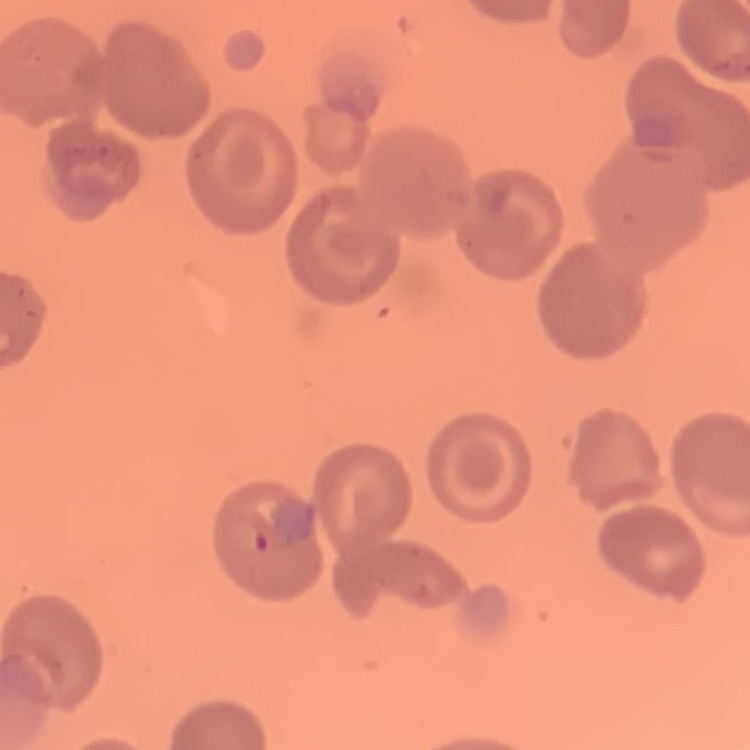
{
  "erythrocyte_morphology": "no rouleaux formation",
  "preparation": "thin blood smear",
  "stain": "Field's or Giemsa",
  "image_type": "square crop of a larger photomicrograph"
}